Outline platelets.
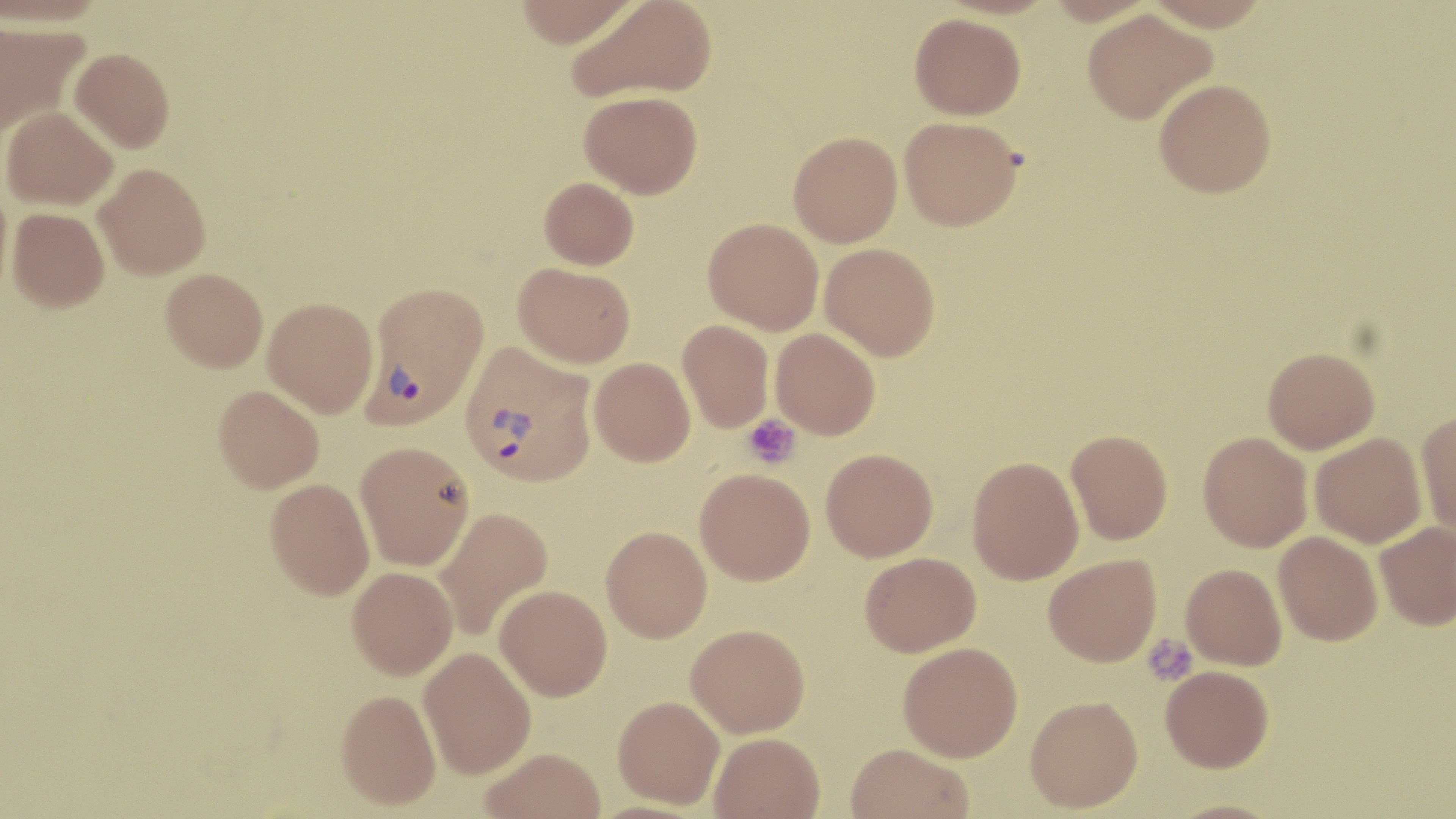
Approximate bounding boxes as (x1, y1, x2, y2) in pixels.
Platelets: (743, 414, 800, 469), (1142, 635, 1197, 685).

Summary:
  - Plasmodium vivax-infected red blood cell locations: (362, 280, 489, 429), (460, 343, 597, 486)
  - Uninfected red blood cell locations: (513, 0, 642, 48), (567, 0, 718, 102), (1144, 0, 1271, 30), (1082, 9, 1217, 123), (909, 13, 1026, 119), (0, 19, 89, 139), (70, 47, 175, 152), (1154, 79, 1276, 198), (580, 90, 703, 198), (2, 106, 118, 210), (899, 116, 1023, 231), (788, 131, 903, 247), (94, 164, 211, 278), (539, 176, 639, 269), (0, 180, 13, 307), (7, 208, 109, 312), (703, 217, 824, 334), (820, 242, 940, 360), (513, 262, 635, 368), (160, 268, 268, 372), (263, 297, 378, 417), (677, 319, 774, 433), (771, 328, 881, 439), (1263, 347, 1380, 453), (589, 357, 695, 466), (213, 384, 324, 493), (1416, 412, 1456, 540), (1066, 429, 1173, 544), (1198, 431, 1313, 552), (1310, 432, 1427, 548), (355, 441, 474, 570), (821, 448, 938, 561), (967, 456, 1084, 584), (695, 468, 815, 585), (265, 478, 374, 599), (432, 506, 553, 640), (1374, 521, 1456, 630), (601, 525, 712, 642), (1274, 531, 1383, 645), (860, 552, 981, 656), (1043, 554, 1161, 666), (1181, 563, 1287, 670), (347, 566, 458, 679), (494, 585, 612, 701), (686, 623, 810, 737), (897, 641, 1023, 761), (419, 647, 536, 778), (1160, 665, 1274, 772), (336, 688, 441, 809), (613, 695, 725, 808), (1024, 695, 1143, 812), (710, 732, 824, 819), (845, 743, 975, 819), (480, 747, 606, 819), (1161, 799, 1286, 819)
  - Slide-level diagnosis: Plasmodium vivax
  - Preparation: thin blood smear
  - Stain: May-Grünwald-Giemsa
  - Magnification: 1000x
  - Modality: optical microscopy
  - Image size: 1456×819 pixels
  - Field of view: one of a larger specimen